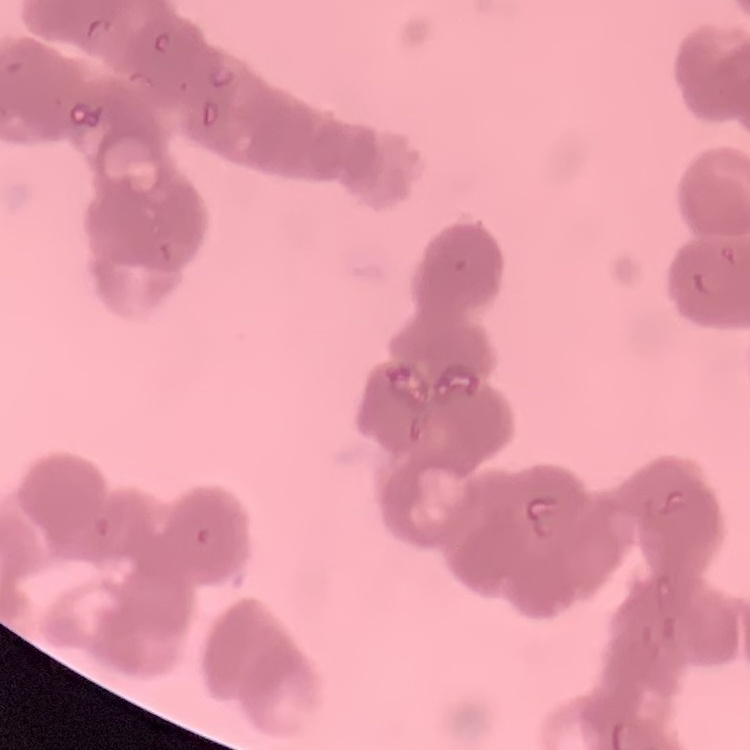

red blood cell morphology = rouleaux formation
preparation = thin blood smear
image type = one tile cut from a larger photomicrograph
stain = Field's or Giemsa